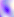
modality = photomicrograph
magnification = 400x
identification = Toxoplasma gondii